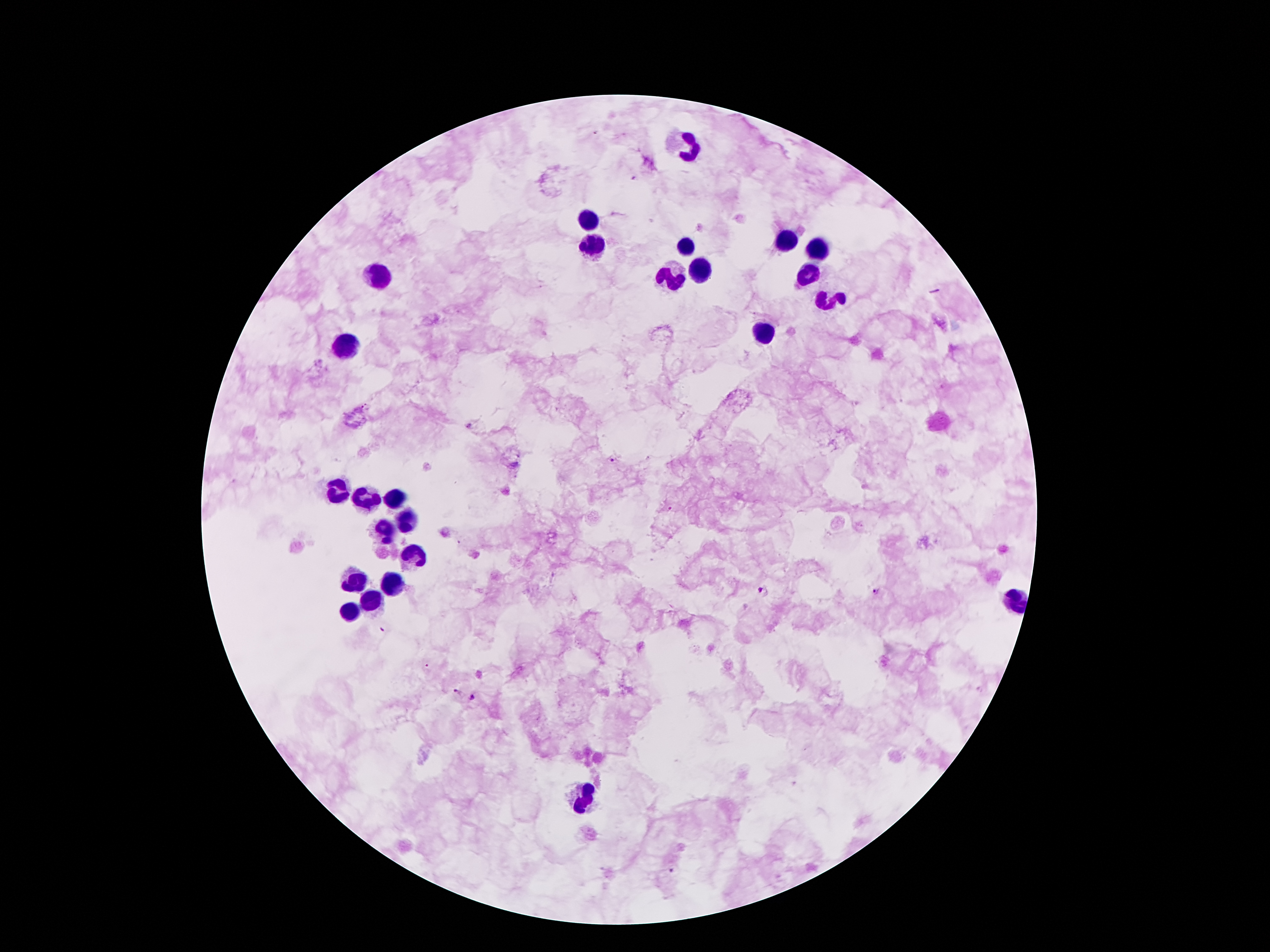
Approximate centers as {x, y} in pixels.
Summary:
  - Leukocyte locations: {689, 145}, {591, 220}, {786, 237}, {594, 244}, {686, 244}, {812, 247}, {697, 268}, {668, 273}, {807, 273}, {379, 275}, {833, 299}, {762, 331}, {348, 342}, {339, 491}, {360, 499}, {398, 499}, {408, 520}, {386, 531}, {416, 554}, {355, 581}, {390, 585}, {1016, 599}, {373, 601}, {353, 614}, {586, 794}
  - Plasmodium parasite locations: {636, 179}, {469, 424}, {614, 459}, {672, 509}, {763, 591}, {877, 591}, {383, 627}, {459, 691}, {473, 697}, {672, 870}
  - Image size: 1270×952 pixels
  - Field of view: one from this slide
  - Capture: smartphone camera through the microscope eyepiece
  - Stain: Giemsa
  - Patient malaria status: positive for Plasmodium falciparum
  - Magnification: 100x
  - Preparation: thick blood film